Describe the morphology of the erythrocytes.
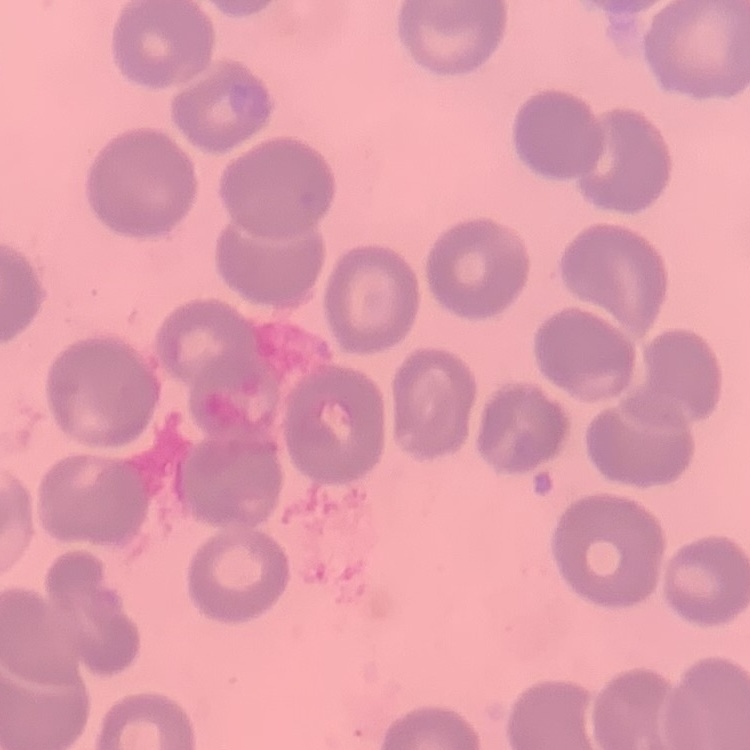
They show no rouleaux formation.

{
  "stain": "Field's or Giemsa",
  "preparation": "thin blood smear",
  "image_type": "square crop of a larger photomicrograph"
}